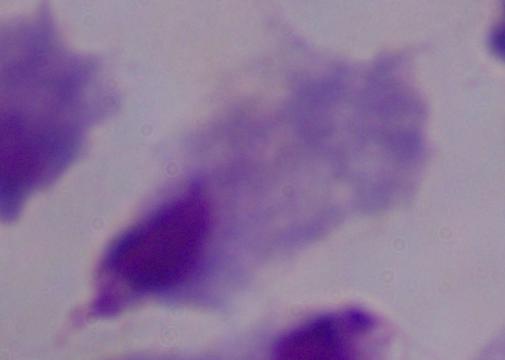
Summary:
  - Magnification: 1000x
  - Modality: micrograph
  - Identification: trichomonad